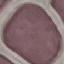

result = negative for malaria parasites
stain = Giemsa
preparation = thin blood smear
image type = cell patch, automatically extracted from a larger field of view and resized to 64 × 64 pixels
capture = smartphone camera at the microscope eyepiece